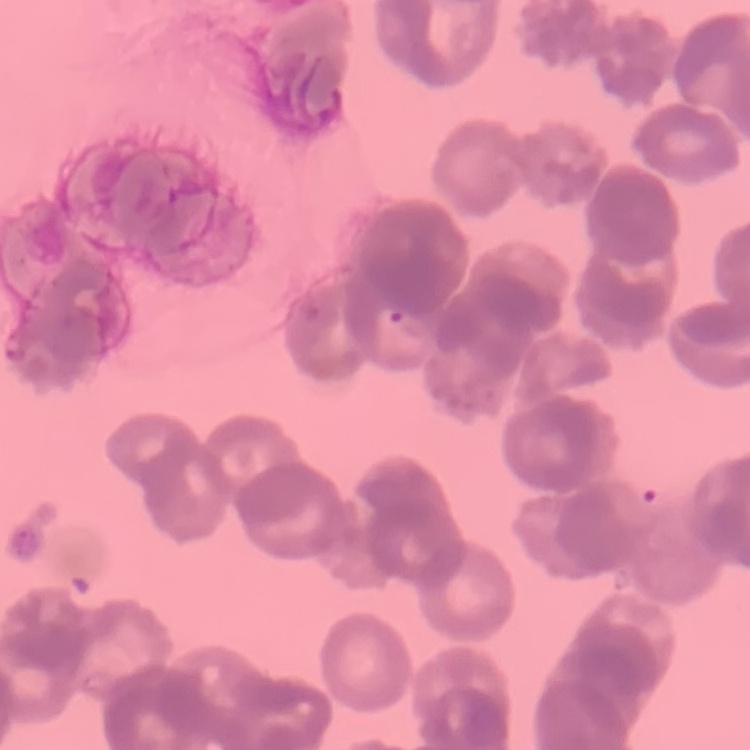

Summary:
  - Red blood cell morphology: rouleaux formation
  - Image type: one tile cut from a larger photomicrograph
  - Preparation: thin blood film
  - Stain: Field's or Giemsa